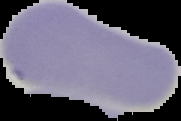
Summary:
  - Preparation: thin blood smear
  - Image size: 181×121 pixels
  - Image type: segmented cell region with the area outside set to black
  - Malaria status: uninfected